Identify the blood parasite species.
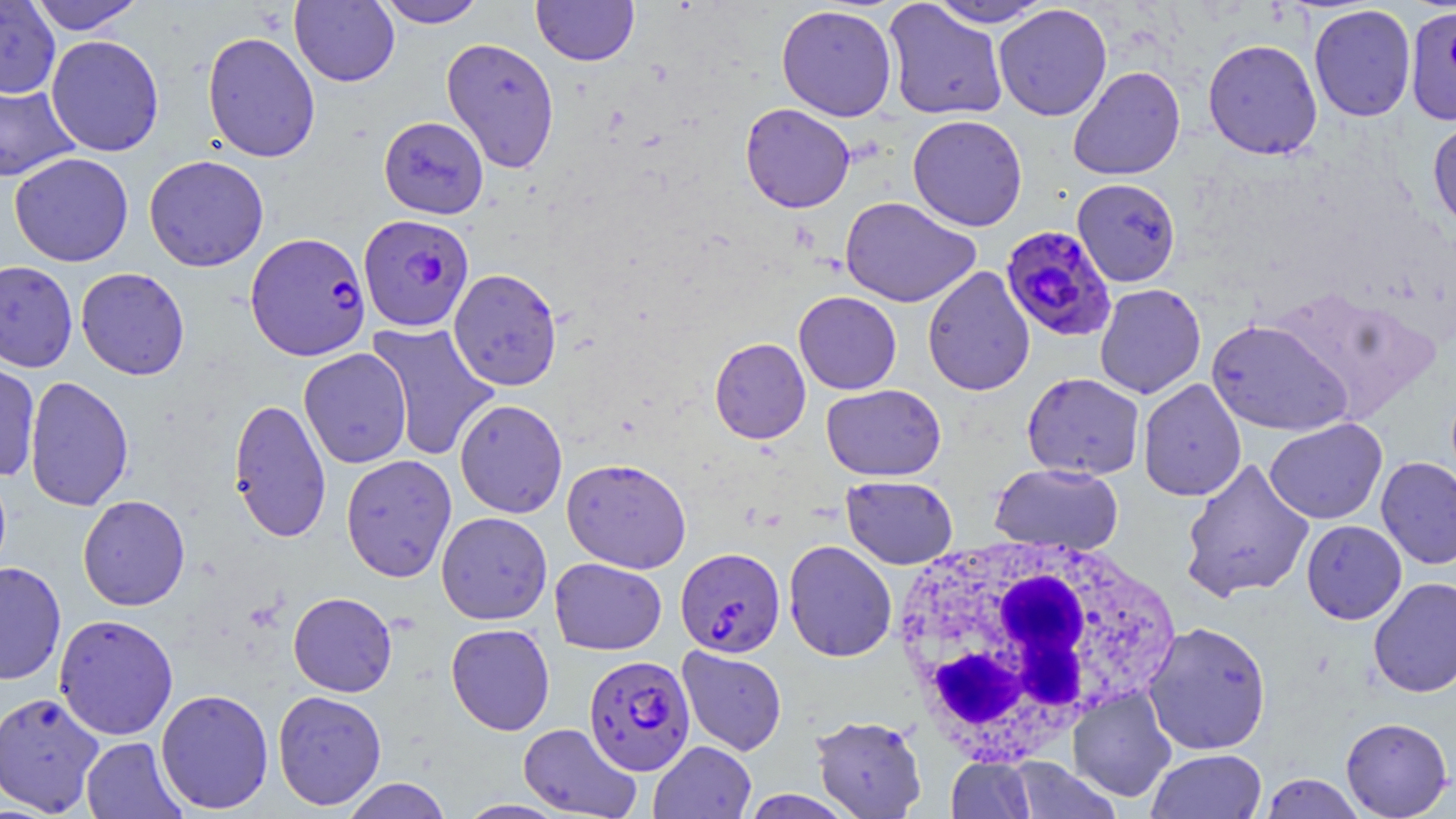

Plasmodium falciparum.

image size = 1456×819 pixels
uninfected red blood cell locations = approximate bounding boxes as named x1/y1/x2/y2 corners in pixels: (x1=28, y1=0, x2=146, y2=35), (x1=290, y1=0, x2=400, y2=87), (x1=374, y1=0, x2=488, y2=28), (x1=531, y1=0, x2=639, y2=66), (x1=0, y1=1, x2=60, y2=98), (x1=882, y1=1, x2=1008, y2=121), (x1=926, y1=1, x2=1053, y2=28), (x1=776, y1=4, x2=898, y2=122), (x1=993, y1=4, x2=1113, y2=121), (x1=1308, y1=4, x2=1417, y2=122), (x1=1405, y1=5, x2=1456, y2=126), (x1=202, y1=31, x2=321, y2=162), (x1=45, y1=34, x2=164, y2=157), (x1=441, y1=37, x2=560, y2=172), (x1=1202, y1=38, x2=1323, y2=160), (x1=1067, y1=66, x2=1185, y2=181), (x1=0, y1=77, x2=81, y2=182), (x1=740, y1=103, x2=855, y2=213), (x1=907, y1=114, x2=1028, y2=231), (x1=378, y1=115, x2=489, y2=218), (x1=1427, y1=116, x2=1456, y2=236), (x1=9, y1=153, x2=134, y2=267), (x1=143, y1=154, x2=269, y2=271), (x1=1072, y1=178, x2=1181, y2=287), (x1=840, y1=196, x2=981, y2=308), (x1=0, y1=260, x2=78, y2=372), (x1=922, y1=266, x2=1035, y2=396), (x1=76, y1=267, x2=190, y2=380), (x1=447, y1=268, x2=563, y2=391), (x1=1094, y1=283, x2=1206, y2=399), (x1=793, y1=291, x2=902, y2=395), (x1=1206, y1=318, x2=1353, y2=436), (x1=365, y1=321, x2=501, y2=462), (x1=709, y1=337, x2=811, y2=444), (x1=299, y1=348, x2=412, y2=469), (x1=0, y1=357, x2=41, y2=480), (x1=1021, y1=372, x2=1145, y2=480), (x1=24, y1=376, x2=133, y2=512), (x1=1138, y1=378, x2=1247, y2=501), (x1=821, y1=383, x2=946, y2=481), (x1=228, y1=397, x2=331, y2=542), (x1=454, y1=399, x2=568, y2=518), (x1=1264, y1=418, x2=1387, y2=524), (x1=340, y1=454, x2=457, y2=582), (x1=1376, y1=456, x2=1456, y2=570), (x1=562, y1=457, x2=691, y2=573), (x1=1179, y1=457, x2=1315, y2=603), (x1=989, y1=462, x2=1124, y2=554), (x1=841, y1=475, x2=958, y2=569), (x1=77, y1=495, x2=190, y2=611), (x1=436, y1=511, x2=552, y2=624), (x1=1301, y1=520, x2=1406, y2=625), (x1=783, y1=540, x2=897, y2=662), (x1=549, y1=558, x2=667, y2=655), (x1=0, y1=561, x2=67, y2=685), (x1=1368, y1=577, x2=1456, y2=698), (x1=288, y1=592, x2=397, y2=697), (x1=53, y1=613, x2=179, y2=740), (x1=1142, y1=620, x2=1272, y2=755), (x1=445, y1=623, x2=555, y2=735), (x1=677, y1=646, x2=787, y2=756), (x1=1068, y1=686, x2=1178, y2=802), (x1=155, y1=688, x2=274, y2=814), (x1=272, y1=690, x2=387, y2=810), (x1=0, y1=691, x2=105, y2=816), (x1=811, y1=714, x2=927, y2=819), (x1=1340, y1=717, x2=1453, y2=818), (x1=518, y1=722, x2=641, y2=819), (x1=80, y1=736, x2=188, y2=819), (x1=649, y1=740, x2=756, y2=819), (x1=1146, y1=748, x2=1267, y2=819), (x1=946, y1=757, x2=1035, y2=819), (x1=1007, y1=760, x2=1121, y2=818), (x1=1259, y1=773, x2=1366, y2=818), (x1=341, y1=777, x2=452, y2=819), (x1=457, y1=800, x2=567, y2=818)
Plasmodium falciparum-infected red blood cell locations = approximate bounding boxes as named x1/y1/x2/y2 corners in pixels: (x1=358, y1=213, x2=474, y2=332), (x1=1000, y1=225, x2=1118, y2=342), (x1=245, y1=232, x2=371, y2=361), (x1=676, y1=547, x2=786, y2=658), (x1=583, y1=654, x2=695, y2=776)
modality = light microscopy
white blood cell locations = approximate bounding boxes as named x1/y1/x2/y2 corners in pixels: (x1=890, y1=533, x2=1173, y2=763)
preparation = thin blood film
stain = May-Grünwald-Giemsa
magnification = 1000x
field of view = one of a larger specimen